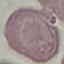 Malaria status: uninfected. Automatically extracted cell patch, resized to 64 × 64 pixels. Giemsa-stained preparation. Thin blood smear. Acquired by smartphone through the microscope eyepiece.